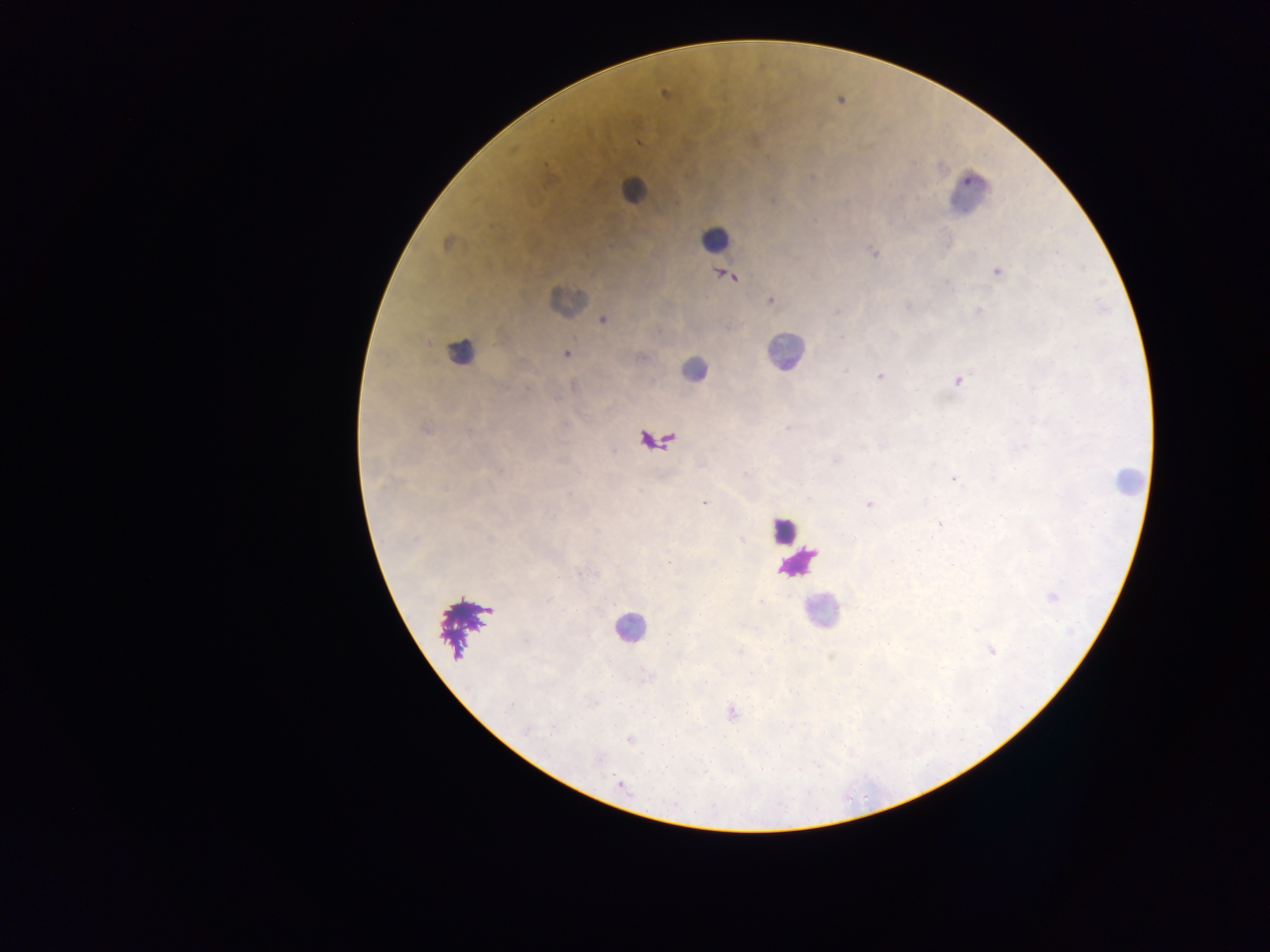

field of view = single
capture = mobile-phone photograph through a microscope
preparation = thick blood film
country = Ghana
leukocyte locations = approximate centers as x y in pixels (subset; some below the resolvable size): 632 190; 970 194; 715 238; 566 300; 784 351; 460 352; 694 369; 1127 479; 782 530; 798 564; 820 611; 466 626; 630 628
malaria parasite locations = approximate centers as x y in pixels: 665 95; 639 142; 817 220; 446 243; 873 252; 998 271; 729 276; 770 301; 908 306; 979 311; 603 320; 567 354; 845 371; 880 376; 957 381; 788 429; 426 430; 883 446; 1024 446; 836 461; 745 474; 954 479; 993 479; 705 503; 868 505; 938 524; 489 539; 741 539; 919 550; 667 562; 578 573; 1053 596; 739 651; 991 651; 593 704; 509 706; 732 714; 552 728; 526 730; 629 740; 622 785
image size = 1270×952 pixels